Assess this cell for malaria.
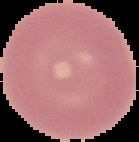
It is uninfected.

{
  "preparation": "thin blood smear",
  "image_size": "139×142 pixels",
  "image_type": "cell region segmented out of the field of view; surrounding area masked to black"
}